Report the malaria status of this cell.
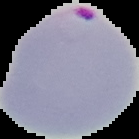
Parasitized.

Image is 139×139 pixels. From a thin blood film. The area outside the segmented cell region is set to black.